Name the parasite shown.
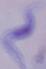
This is a trypanosome.

Summary:
  - Modality: micrograph
  - Magnification: 1000x